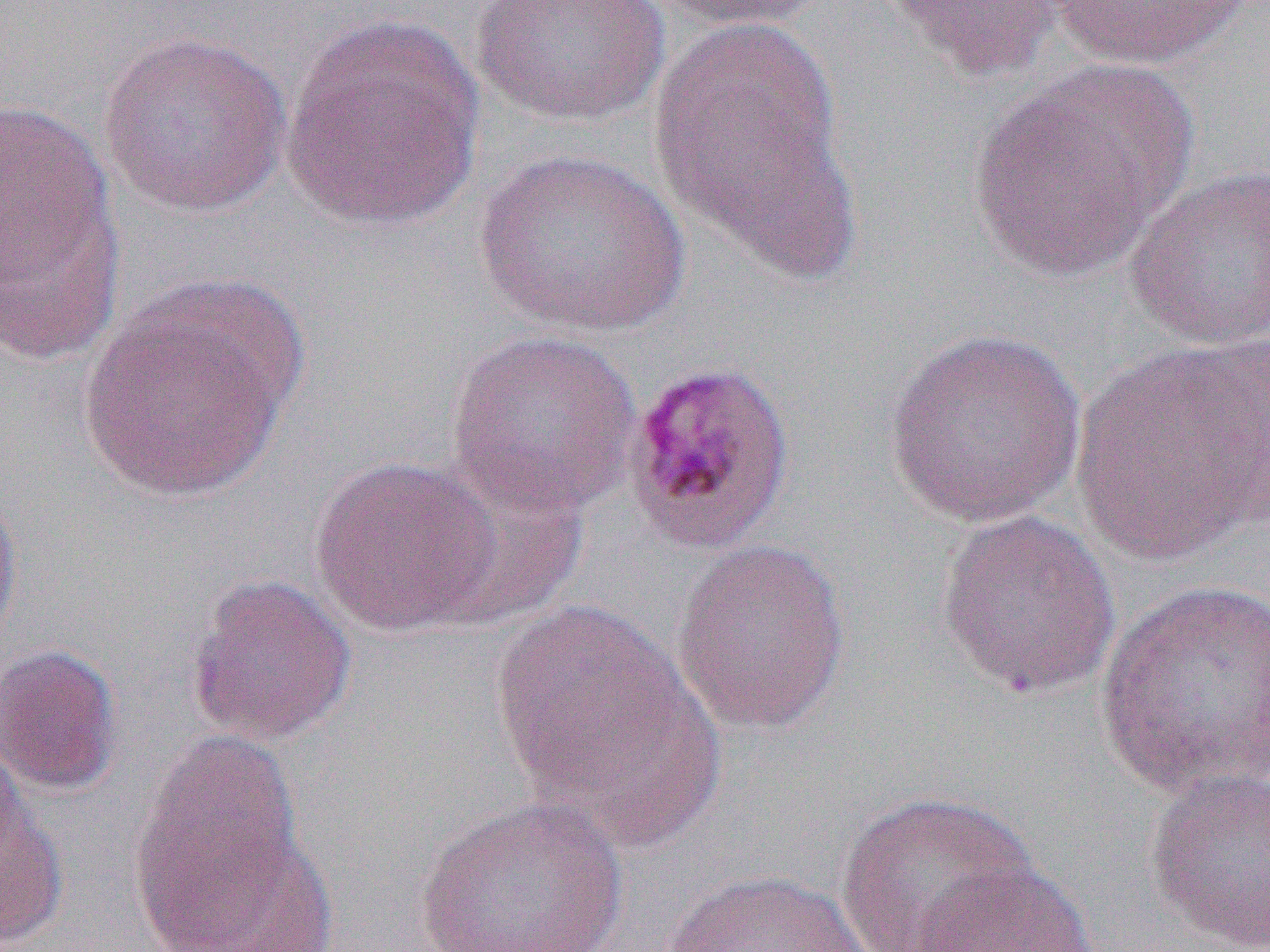

Summary:
  - Coordinate format: approximate bounding boxes as (x1, y1, x2, y2) in pixels
  - Uninfected red blood cell locations: (468, 0, 672, 128), (652, 0, 836, 32), (884, 0, 1068, 84), (1042, 0, 1258, 70), (281, 13, 486, 230), (647, 15, 856, 276), (98, 29, 292, 218), (969, 63, 1194, 282), (0, 98, 116, 300), (472, 146, 692, 338), (1124, 164, 1270, 352), (1, 178, 125, 365), (78, 298, 294, 504), (882, 326, 1089, 527), (444, 328, 643, 519), (1073, 338, 1267, 565), (310, 455, 505, 637), (420, 463, 588, 632), (0, 481, 23, 658), (935, 509, 1122, 701), (670, 537, 852, 737), (185, 574, 358, 747), (1094, 576, 1270, 797), (489, 599, 706, 820), (0, 643, 124, 796), (131, 728, 309, 945), (0, 732, 34, 878), (1143, 767, 1270, 951), (0, 780, 67, 951), (834, 790, 1035, 952), (413, 795, 631, 952), (154, 823, 338, 952), (903, 861, 1099, 952), (657, 869, 873, 952)
  - Plasmodium malariae-infected red blood cell locations: (619, 357, 796, 556)
  - Slide-level diagnosis: Plasmodium malariae
  - Modality: optical microscopy
  - Magnification: 1000x
  - Preparation: thin blood smear
  - Image size: 1270×952 pixels
  - Field of view: single